Identify the malaria species.
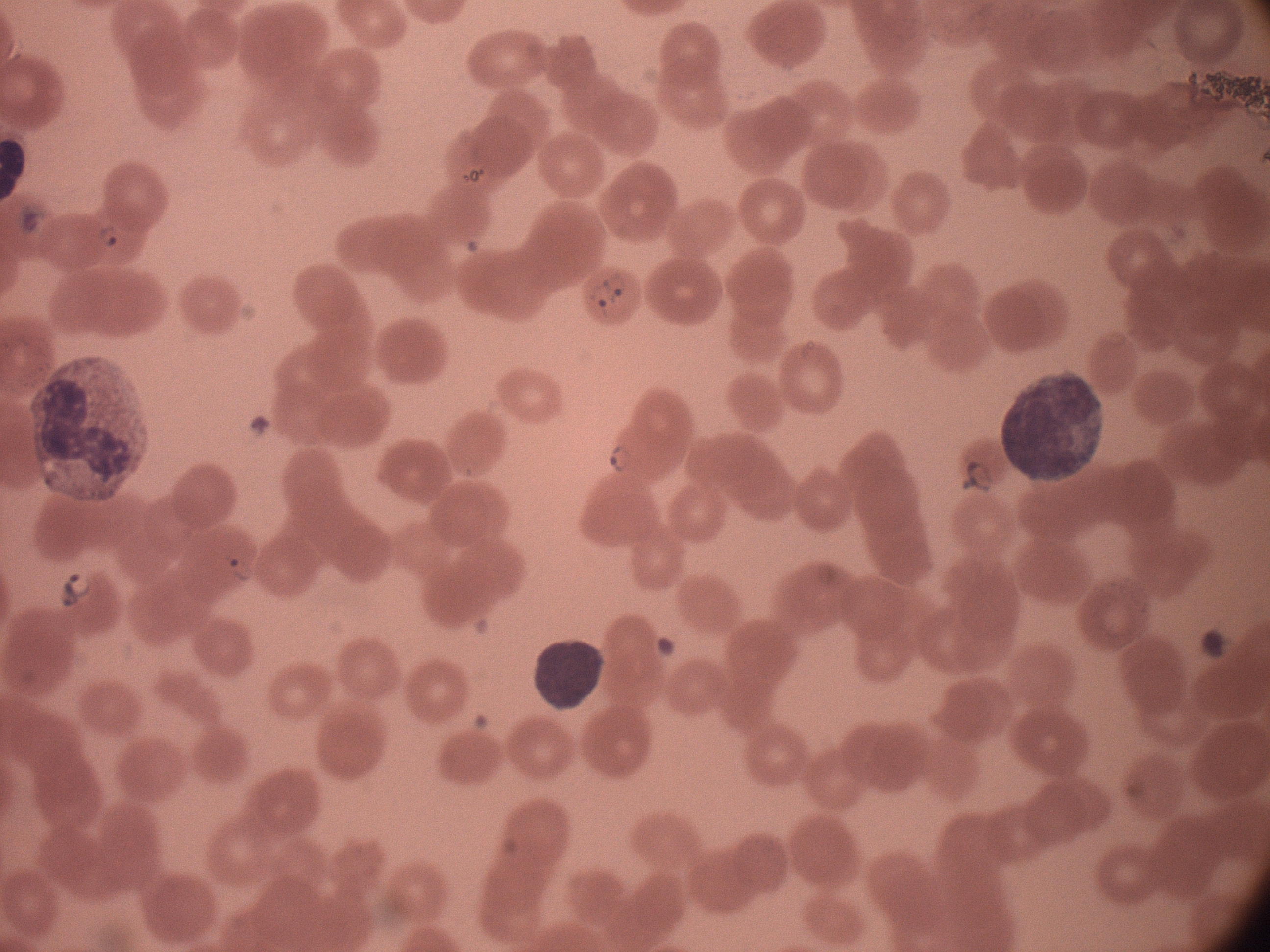

Plasmodium falciparum.

Approximate bounding boxes as (x1, y1, x2, y2) in pixels, from the source annotation, which is not necessarily exhaustive.
Summary:
  - Ring form locations: (93, 217, 127, 251), (604, 268, 634, 308), (578, 276, 622, 327), (602, 436, 637, 479), (949, 445, 999, 500), (221, 537, 264, 587), (51, 562, 98, 614)
  - Microscope: Leica DM2000 with built-in camera
  - Magnification: 100x
  - Stain: Giemsa
  - Image size: 1270×952 pixels
  - Field of view: one from this slide
  - Preparation: thin blood film